Identify the parasite.
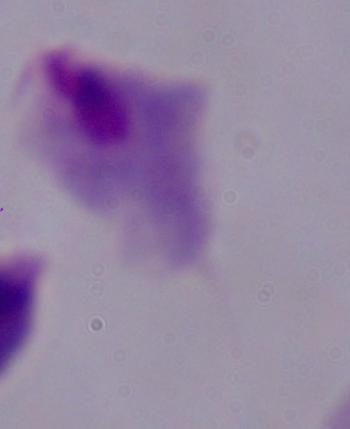
A trichomonad.

Captured at 1000x magnification. Photomicrograph.